Assess the morphology of the red blood cells.
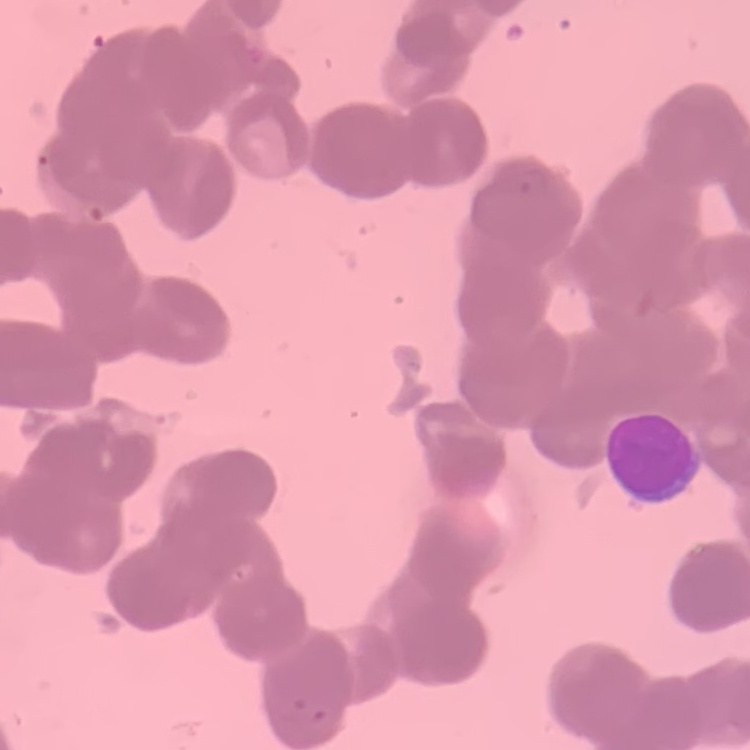

Rouleaux formation.

Summary:
  - Preparation: thin blood film
  - Stain: Field's or Giemsa
  - Image type: square crop of a larger photomicrograph